State the preparation type.
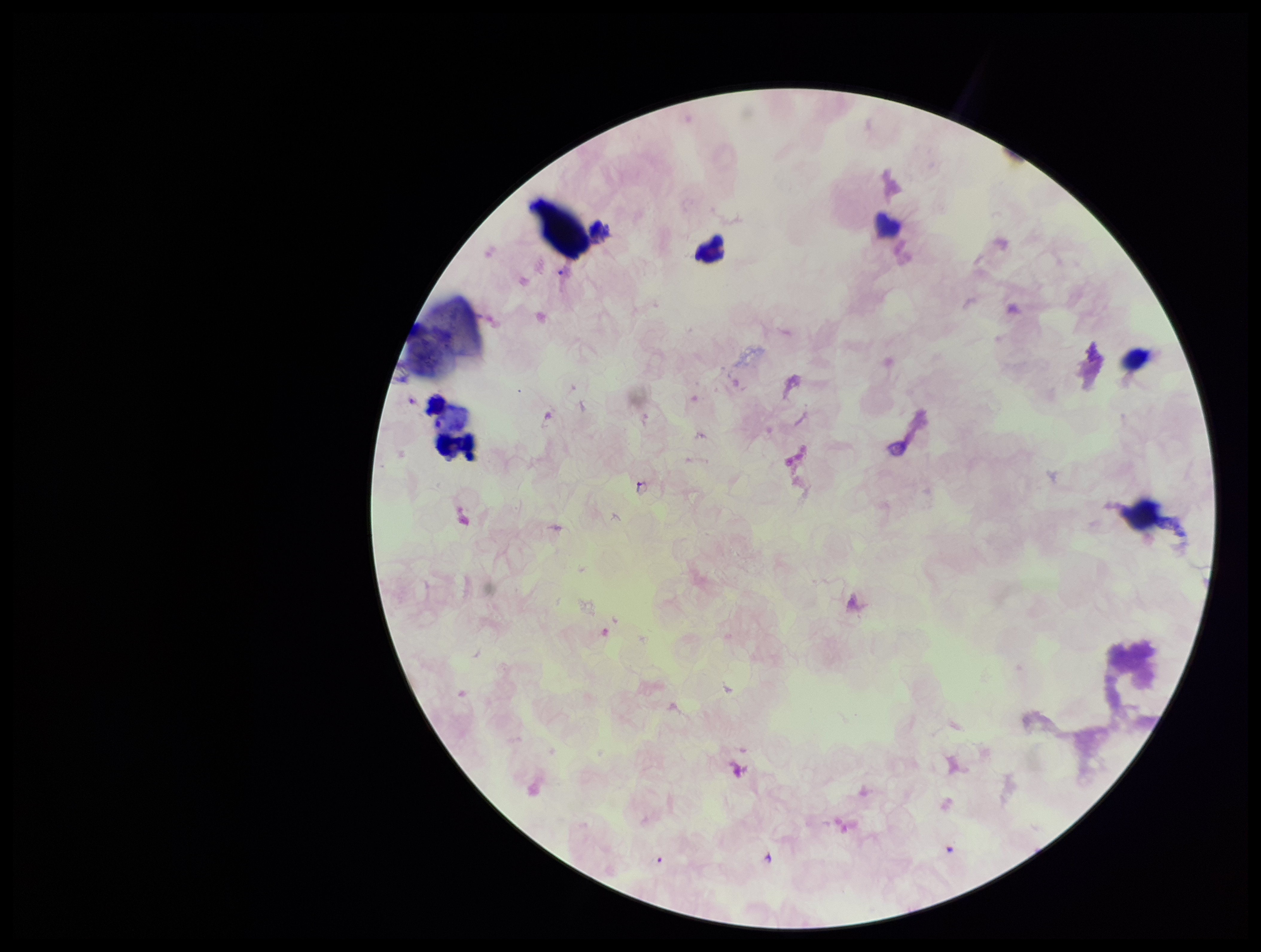

Thick.

{
  "stain": "Giemsa",
  "species_reported_for_this_patient": "Plasmodium falciparum",
  "image_size": "1261×952 pixels",
  "field_of_view": "one from this slide",
  "plasmodium_parasites": "identified",
  "patient_malaria_status": "positive",
  "leukocyte_count": 2,
  "capture": "smartphone photograph through the microscope eyepiece",
  "parasite_count": 3
}